Assess this cell for malaria.
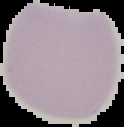

Uninfected.

{
  "image_size": "124×127 pixels",
  "preparation": "thin blood smear",
  "image_type": "segmented cell region with the area outside set to black"
}